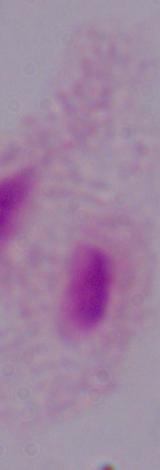
A trichomonad is seen. Micrograph. 1000x magnification.